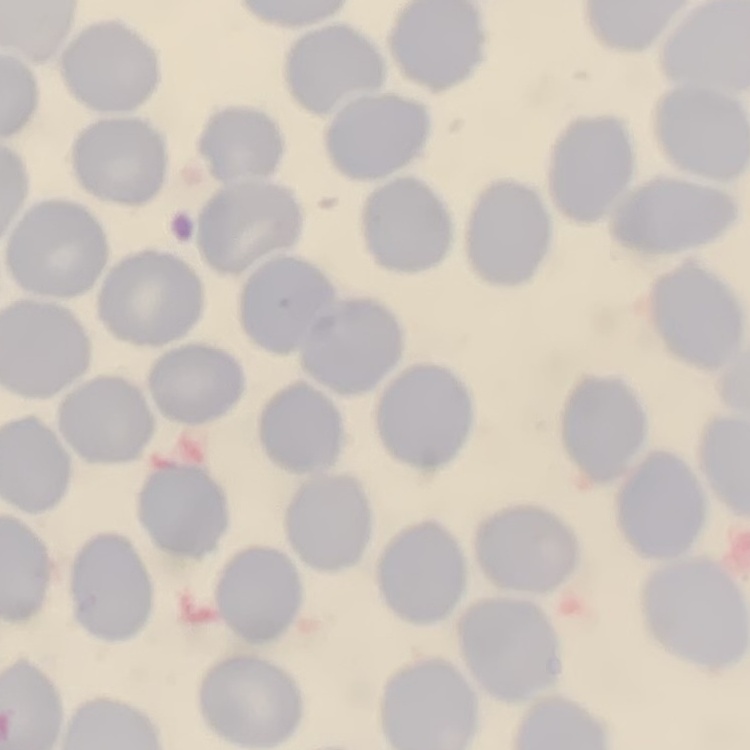

erythrocyte morphology = no rouleaux formation
stain = Field's or Giemsa
preparation = thin blood smear
image type = one tile cut from a larger photomicrograph